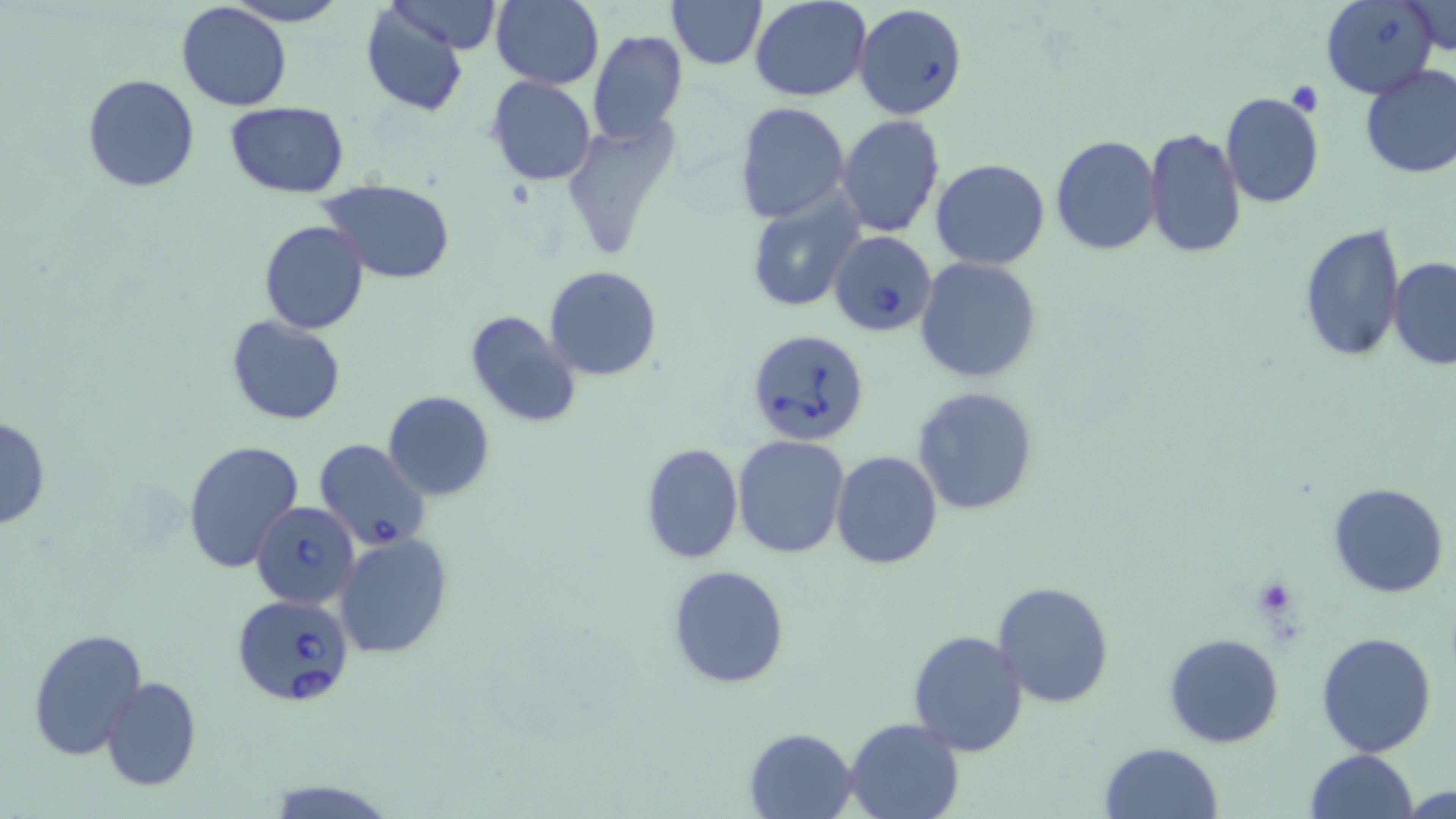 Approximate bounding boxes as (x1, y1, x2, y2) in pixels. Uninfected red blood cell locations: (220, 0, 351, 26), (388, 0, 504, 55), (492, 0, 605, 89), (667, 0, 767, 69), (750, 1, 873, 102), (175, 3, 292, 111), (1402, 3, 1453, 56), (360, 4, 469, 116), (587, 29, 688, 145), (1359, 65, 1456, 181), (81, 73, 200, 192), (487, 76, 596, 186), (1220, 91, 1326, 209), (734, 101, 851, 223), (225, 102, 349, 197), (837, 114, 945, 238), (560, 121, 678, 259), (1143, 128, 1244, 260), (1050, 135, 1162, 256), (932, 159, 1050, 270), (319, 179, 456, 283), (745, 194, 862, 311), (259, 221, 370, 335), (1298, 221, 1406, 362), (1387, 256, 1456, 370), (915, 257, 1042, 385), (544, 266, 664, 381), (464, 311, 582, 427), (226, 316, 345, 424), (910, 385, 1039, 517), (383, 390, 495, 500), (0, 414, 50, 531), (733, 435, 850, 557), (181, 439, 303, 574), (639, 442, 744, 565), (831, 450, 942, 569), (1329, 482, 1449, 598), (335, 534, 453, 659), (666, 564, 789, 689), (992, 580, 1115, 708), (25, 627, 147, 761), (907, 628, 1031, 756), (1316, 631, 1437, 757), (1163, 632, 1286, 749), (100, 675, 202, 790), (844, 717, 965, 819), (743, 726, 859, 817), (1099, 742, 1224, 819), (1303, 749, 1418, 819), (1401, 783, 1455, 818). Babesia divergens-infected red blood cell locations: (1321, 0, 1440, 99), (852, 2, 968, 121), (829, 231, 936, 336), (748, 328, 871, 450), (314, 436, 430, 553), (252, 501, 361, 608), (232, 593, 354, 706). Platelet locations: (1287, 81, 1323, 116), (1251, 576, 1302, 627). Slide-level diagnosis: Babesia divergens. May-Grünwald-Giemsa-stained preparation. Image is 1456×819 pixels. Optical microscopy. Captured at 1000x magnification. Single field of view. Thin blood smear.